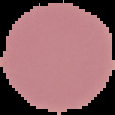

{
  "image_type": "segmented cell region with the area outside set to black",
  "result": "no malaria parasites seen",
  "image_size": "115×115 pixels",
  "preparation": "thin blood film"
}